Classify this cell by malaria status.
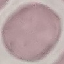
Uninfected.

Summary:
  - Image type: cell patch, automatically extracted from a larger field of view and resized to 64 × 64 pixels
  - Stain: Giemsa
  - Preparation: thin blood film
  - Capture: smartphone camera at the microscope eyepiece